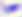
Toxoplasma gondii is shown. Photomicrograph. Captured at 400x magnification.